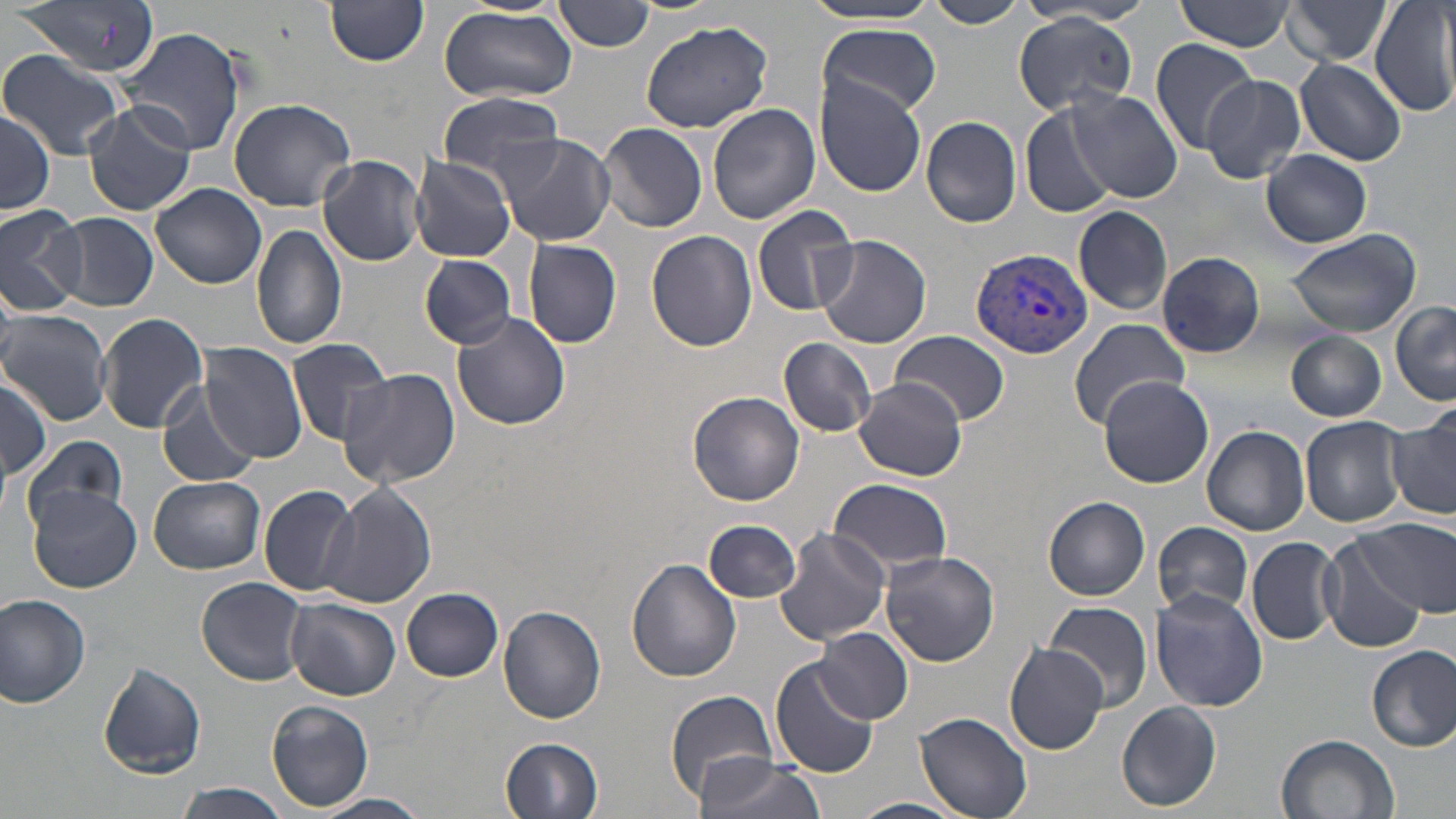

slide_level_diagnosis: Plasmodium vivax
modality: light microscopy
stain: May-Grünwald-Giemsa
field_of_view: one of a larger specimen
image_size: 1456×819 pixels
magnification: 1000x
uninfected_red_blood_cell_locations: 'approximate bounding boxes as [x1, y1, x2, y2] in pixels: [15, 0, 160, 78], [324, 0, 430, 67], [555, 0, 656, 52], [922, 0, 1027, 27], [1176, 0, 1293, 51], [1281, 0, 1395, 65], [796, 1, 945, 26], [1371, 3, 1456, 119], [440, 7, 578, 104], [1014, 15, 1138, 116], [639, 20, 771, 132], [818, 22, 942, 117], [119, 29, 241, 157], [1149, 37, 1259, 151], [1, 48, 125, 160], [1293, 57, 1407, 165], [1199, 74, 1305, 183], [816, 77, 926, 196], [1069, 90, 1184, 202], [438, 92, 564, 185], [228, 97, 358, 211], [83, 101, 195, 216], [1021, 102, 1127, 224], [708, 103, 820, 225], [0, 109, 54, 216], [921, 115, 1022, 229], [599, 123, 708, 234], [497, 134, 616, 245], [1260, 150, 1373, 248], [318, 156, 426, 266], [410, 157, 518, 262], [152, 183, 267, 289], [753, 204, 859, 318], [0, 206, 87, 316], [1072, 206, 1173, 316], [55, 213, 158, 311], [251, 224, 348, 351], [645, 229, 757, 352], [1284, 230, 1423, 337], [813, 234, 932, 350], [524, 238, 623, 348], [1156, 252, 1266, 357], [421, 256, 517, 349], [1390, 301, 1456, 408], [1, 309, 113, 425], [451, 313, 570, 432], [98, 314, 209, 432], [1064, 320, 1190, 433], [888, 331, 1011, 425], [1285, 332, 1387, 421], [779, 337, 878, 437], [285, 338, 396, 444], [198, 341, 308, 464], [336, 367, 462, 490], [856, 377, 965, 481], [1099, 377, 1213, 488], [0, 379, 51, 482], [157, 384, 258, 488], [688, 391, 803, 505], [1385, 412, 1456, 522], [1300, 416, 1408, 528], [1202, 426, 1310, 536], [23, 435, 128, 533], [149, 476, 266, 574], [829, 478, 952, 572], [323, 482, 437, 608], [260, 484, 361, 599], [28, 485, 140, 594], [1043, 496, 1150, 600], [704, 519, 802, 603], [1357, 519, 1456, 616], [1152, 521, 1254, 618], [775, 527, 891, 646], [1319, 534, 1428, 653], [1247, 538, 1341, 646], [879, 550, 999, 666], [627, 558, 742, 683], [198, 577, 309, 685], [401, 587, 503, 681], [1149, 590, 1270, 711], [0, 592, 93, 709], [286, 598, 400, 700], [1044, 599, 1152, 713], [498, 606, 605, 725], [818, 626, 912, 722], [1005, 644, 1108, 755], [1367, 644, 1456, 753], [770, 658, 879, 777], [96, 663, 206, 777], [669, 687, 784, 802], [266, 700, 373, 811], [1117, 701, 1223, 812], [915, 712, 1032, 818], [1276, 732, 1400, 819], [500, 736, 604, 818], [697, 756, 827, 819], [176, 781, 291, 819], [315, 793, 430, 819], [849, 796, 965, 819]'
preparation: thin blood smear
plasmodium_vivax_infected_red_blood_cell_locations: 'approximate bounding boxes as [x1, y1, x2, y2] in pixels: [970, 246, 1095, 358]'